Give the extent of all uninfected red blood cells.
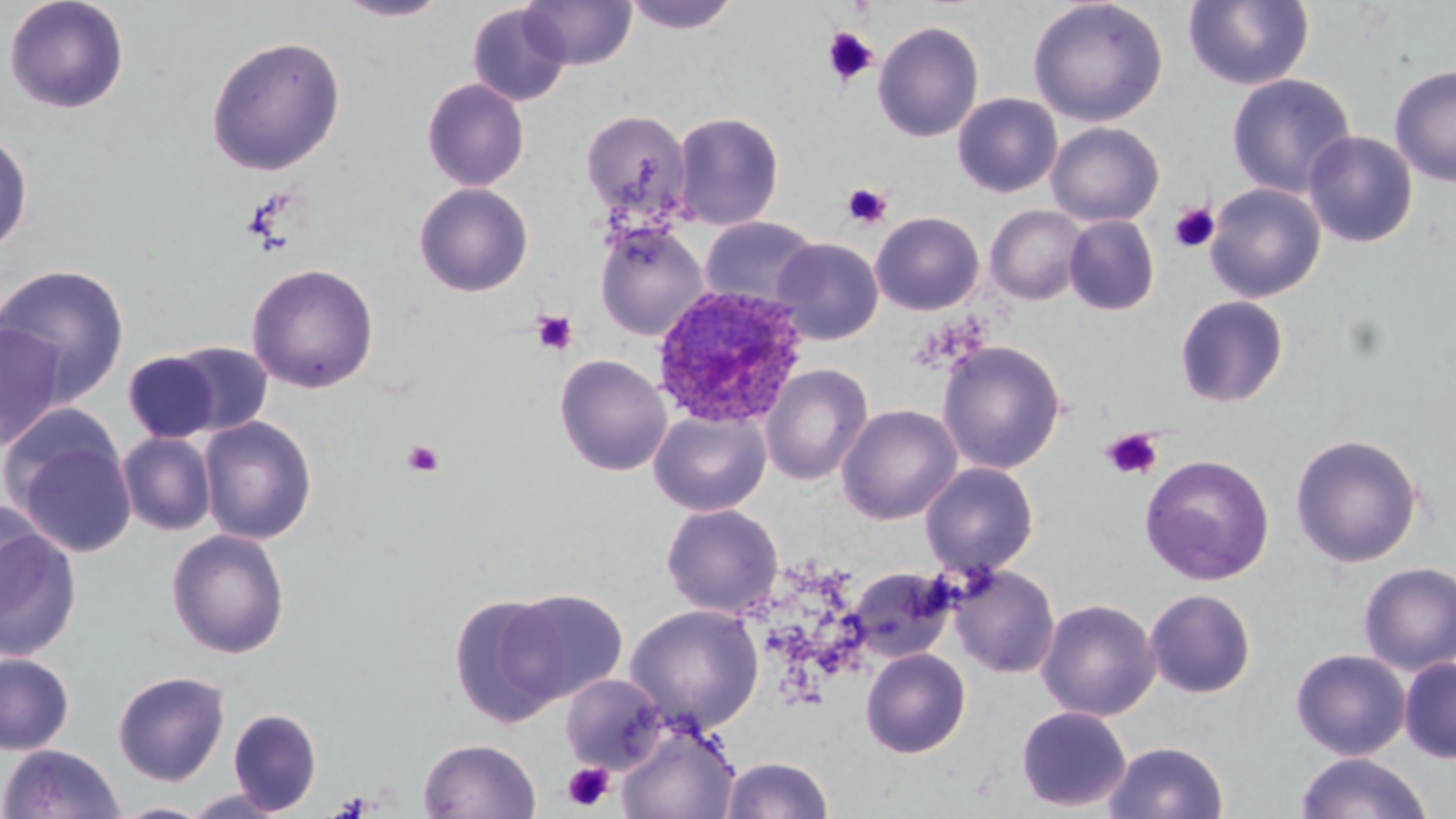

Approximate bounding boxes as (x1, y1, x2, y2) in pixels.
Uninfected red blood cells: (2, 0, 131, 115), (333, 0, 451, 22), (520, 0, 637, 70), (621, 0, 742, 34), (1027, 0, 1168, 127), (1183, 0, 1314, 91), (467, 3, 571, 107), (873, 21, 984, 143), (205, 34, 346, 176), (1389, 64, 1456, 187), (1225, 73, 1358, 199), (421, 77, 530, 191), (952, 93, 1063, 198), (580, 109, 692, 221), (672, 111, 785, 231), (1046, 121, 1164, 226), (0, 129, 34, 255), (1303, 131, 1418, 247), (413, 182, 534, 297), (1205, 183, 1326, 302), (985, 205, 1089, 306), (870, 211, 985, 315), (1064, 215, 1160, 316), (699, 216, 821, 309), (594, 222, 708, 341), (772, 237, 883, 345), (1, 263, 132, 402), (246, 263, 380, 394), (1174, 295, 1289, 408), (0, 322, 67, 451), (936, 340, 1066, 474), (167, 341, 275, 437), (123, 350, 221, 443), (554, 354, 672, 476), (760, 363, 873, 486), (836, 403, 962, 525), (649, 409, 771, 516), (3, 410, 139, 559), (198, 416, 318, 544), (117, 432, 216, 535), (1290, 432, 1423, 568), (1139, 453, 1275, 585), (920, 462, 1039, 579), (0, 500, 51, 624), (661, 503, 784, 617), (0, 511, 83, 662), (166, 528, 290, 658), (1359, 562, 1456, 674), (950, 564, 1060, 678), (848, 566, 958, 663), (497, 587, 629, 706), (1144, 588, 1257, 698), (449, 594, 572, 726), (1036, 598, 1161, 722), (624, 603, 765, 733), (860, 648, 972, 758), (1291, 649, 1411, 760), (0, 651, 75, 755), (1399, 657, 1456, 763), (113, 670, 230, 785), (560, 674, 667, 773), (1015, 705, 1131, 812), (228, 708, 322, 815), (617, 720, 740, 819), (418, 738, 541, 819), (1103, 740, 1230, 819), (0, 744, 125, 818), (1296, 752, 1432, 819), (722, 756, 834, 818), (183, 788, 291, 819), (112, 802, 214, 818).

Summary:
  - Platelet locations: (819, 27, 879, 88), (841, 183, 891, 229), (1168, 202, 1220, 253), (531, 310, 578, 355), (1101, 426, 1164, 481), (402, 439, 443, 477), (562, 761, 615, 811)
  - Plasmodium ovale-infected red blood cell locations: (650, 285, 809, 430)
  - Slide-level diagnosis: Plasmodium ovale
  - Stain: May-Grünwald-Giemsa
  - Magnification: 1000x
  - Field of view: single
  - Image size: 1456×819 pixels
  - Modality: optical microscopy
  - Preparation: thin blood film